Identify the cell.
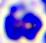
This is a leukocyte.

Photomicrograph. 400x magnification.